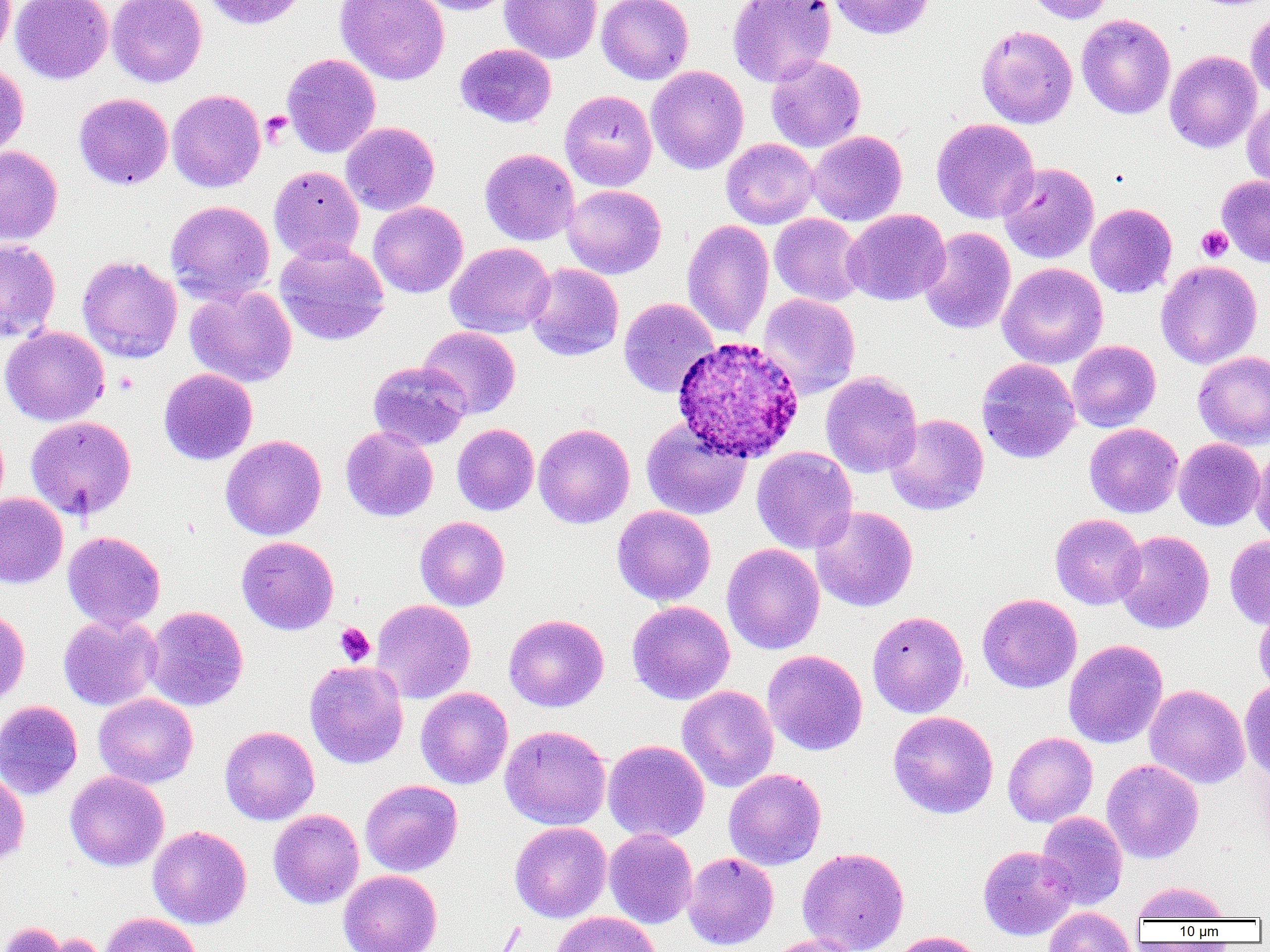

slide-level diagnosis = Plasmodium ovale
uninfected red blood cell locations = approximate bounding boxes as named x1/y1/x2/y2 corners in pixels: (x1=0, y1=0, x2=14, y2=61), (x1=11, y1=0, x2=113, y2=84), (x1=107, y1=0, x2=207, y2=88), (x1=202, y1=0, x2=308, y2=29), (x1=335, y1=0, x2=450, y2=85), (x1=412, y1=0, x2=517, y2=15), (x1=499, y1=0, x2=602, y2=64), (x1=596, y1=0, x2=694, y2=84), (x1=728, y1=0, x2=836, y2=87), (x1=828, y1=0, x2=934, y2=40), (x1=1025, y1=0, x2=1114, y2=24), (x1=1246, y1=7, x2=1270, y2=101), (x1=1076, y1=14, x2=1176, y2=119), (x1=976, y1=25, x2=1078, y2=129), (x1=455, y1=43, x2=557, y2=127), (x1=1164, y1=50, x2=1261, y2=153), (x1=281, y1=53, x2=381, y2=157), (x1=766, y1=54, x2=866, y2=152), (x1=0, y1=61, x2=28, y2=160), (x1=646, y1=66, x2=749, y2=174), (x1=167, y1=89, x2=266, y2=193), (x1=560, y1=90, x2=657, y2=191), (x1=74, y1=92, x2=173, y2=190), (x1=1242, y1=97, x2=1270, y2=193), (x1=931, y1=118, x2=1039, y2=224), (x1=340, y1=121, x2=440, y2=216), (x1=808, y1=130, x2=907, y2=226), (x1=721, y1=138, x2=819, y2=229), (x1=0, y1=146, x2=63, y2=244), (x1=480, y1=148, x2=580, y2=245), (x1=997, y1=162, x2=1099, y2=264), (x1=269, y1=166, x2=364, y2=264), (x1=1217, y1=176, x2=1270, y2=266), (x1=562, y1=185, x2=666, y2=279), (x1=166, y1=200, x2=274, y2=304), (x1=368, y1=201, x2=468, y2=298), (x1=1085, y1=203, x2=1177, y2=298), (x1=843, y1=209, x2=951, y2=305), (x1=769, y1=213, x2=866, y2=306), (x1=682, y1=220, x2=774, y2=339), (x1=919, y1=227, x2=1016, y2=334), (x1=0, y1=239, x2=61, y2=342), (x1=274, y1=242, x2=390, y2=346), (x1=445, y1=242, x2=555, y2=338), (x1=77, y1=255, x2=183, y2=363), (x1=1156, y1=261, x2=1262, y2=368), (x1=997, y1=262, x2=1108, y2=369), (x1=525, y1=263, x2=624, y2=361), (x1=184, y1=285, x2=297, y2=387), (x1=758, y1=293, x2=860, y2=399), (x1=618, y1=297, x2=719, y2=397), (x1=0, y1=325, x2=109, y2=426), (x1=419, y1=326, x2=520, y2=419), (x1=1067, y1=340, x2=1161, y2=431), (x1=1193, y1=351, x2=1270, y2=449), (x1=977, y1=358, x2=1081, y2=464), (x1=367, y1=360, x2=471, y2=451), (x1=158, y1=368, x2=258, y2=465), (x1=820, y1=371, x2=922, y2=478), (x1=885, y1=413, x2=989, y2=515), (x1=26, y1=415, x2=137, y2=520), (x1=641, y1=419, x2=752, y2=520), (x1=452, y1=423, x2=539, y2=516), (x1=533, y1=423, x2=635, y2=529), (x1=1085, y1=423, x2=1183, y2=518), (x1=340, y1=426, x2=438, y2=521), (x1=220, y1=435, x2=326, y2=540), (x1=1173, y1=438, x2=1265, y2=531), (x1=1250, y1=445, x2=1270, y2=548), (x1=752, y1=446, x2=858, y2=554), (x1=0, y1=492, x2=68, y2=588), (x1=612, y1=505, x2=716, y2=606), (x1=810, y1=506, x2=918, y2=612), (x1=1050, y1=513, x2=1146, y2=610), (x1=415, y1=516, x2=510, y2=611), (x1=1113, y1=530, x2=1214, y2=633), (x1=62, y1=531, x2=166, y2=631), (x1=1225, y1=535, x2=1270, y2=629), (x1=236, y1=536, x2=339, y2=634), (x1=722, y1=543, x2=825, y2=654), (x1=977, y1=593, x2=1082, y2=693), (x1=370, y1=599, x2=475, y2=703), (x1=1254, y1=600, x2=1270, y2=697), (x1=627, y1=601, x2=735, y2=705), (x1=144, y1=606, x2=249, y2=711), (x1=0, y1=608, x2=30, y2=709), (x1=867, y1=610, x2=969, y2=718), (x1=503, y1=613, x2=609, y2=712), (x1=58, y1=614, x2=162, y2=711), (x1=1063, y1=639, x2=1168, y2=748), (x1=762, y1=650, x2=867, y2=756), (x1=304, y1=660, x2=408, y2=769), (x1=1240, y1=679, x2=1270, y2=781), (x1=1144, y1=684, x2=1250, y2=789), (x1=677, y1=685, x2=779, y2=791), (x1=416, y1=687, x2=513, y2=789), (x1=93, y1=693, x2=198, y2=788), (x1=0, y1=700, x2=83, y2=799), (x1=888, y1=710, x2=998, y2=818), (x1=219, y1=725, x2=319, y2=825), (x1=500, y1=725, x2=611, y2=830), (x1=1002, y1=732, x2=1098, y2=827), (x1=603, y1=739, x2=710, y2=843), (x1=1102, y1=758, x2=1203, y2=863), (x1=723, y1=768, x2=826, y2=870), (x1=65, y1=771, x2=169, y2=871), (x1=0, y1=773, x2=29, y2=866), (x1=360, y1=779, x2=463, y2=876), (x1=268, y1=809, x2=364, y2=909), (x1=1036, y1=811, x2=1128, y2=909), (x1=509, y1=821, x2=611, y2=922), (x1=147, y1=825, x2=251, y2=928), (x1=604, y1=829, x2=698, y2=928), (x1=978, y1=846, x2=1078, y2=940), (x1=797, y1=847, x2=910, y2=952), (x1=682, y1=851, x2=778, y2=950), (x1=338, y1=869, x2=442, y2=952), (x1=1131, y1=881, x2=1231, y2=922), (x1=1043, y1=906, x2=1137, y2=952), (x1=551, y1=911, x2=662, y2=952), (x1=100, y1=912, x2=202, y2=952), (x1=33, y1=931, x2=111, y2=952), (x1=888, y1=931, x2=986, y2=952), (x1=764, y1=934, x2=864, y2=952)
image size = 1270×952 pixels
field of view = single
preparation = thin blood film
Plasmodium ovale-infected red blood cell locations = approximate bounding boxes as named x1/y1/x2/y2 corners in pixels: (x1=672, y1=335, x2=805, y2=462)
modality = optical microscopy
magnification = 1000x
platelet locations = approximate bounding boxes as named x1/y1/x2/y2 corners in pixels: (x1=260, y1=111, x2=291, y2=147), (x1=1197, y1=226, x2=1233, y2=262), (x1=335, y1=623, x2=375, y2=666)